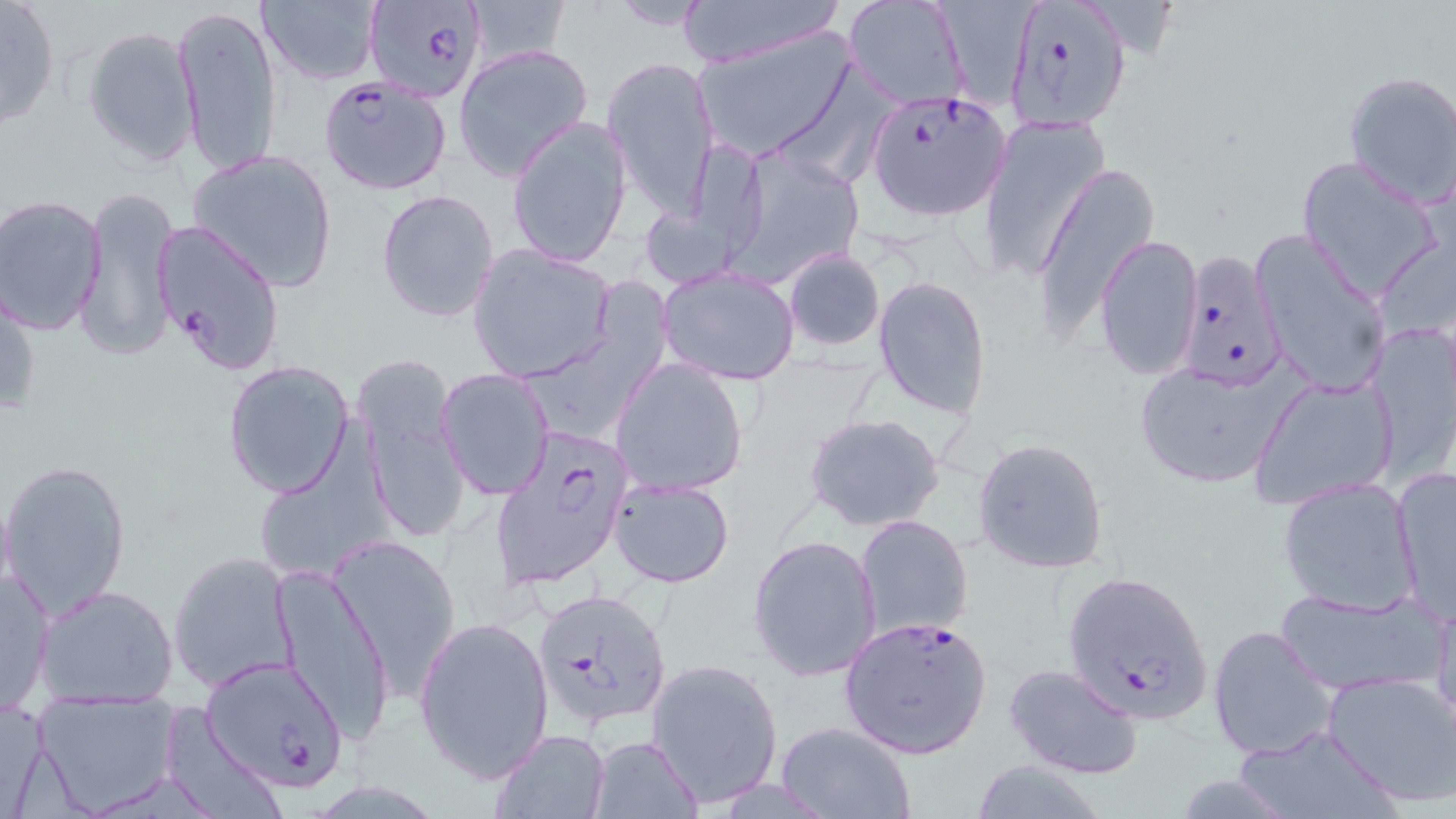

Summary:
  - Coordinate format: approximate bounding boxes as named x1/y1/x2/y2 corners in pixels
  - Uninfected red blood cell locations: (x1=0, y1=0, x2=62, y2=131), (x1=464, y1=0, x2=575, y2=66), (x1=606, y1=0, x2=715, y2=31), (x1=672, y1=0, x2=846, y2=68), (x1=842, y1=0, x2=972, y2=111), (x1=256, y1=1, x2=383, y2=86), (x1=930, y1=2, x2=1055, y2=113), (x1=172, y1=3, x2=282, y2=181), (x1=81, y1=25, x2=203, y2=168), (x1=694, y1=28, x2=857, y2=161), (x1=453, y1=45, x2=594, y2=180), (x1=603, y1=55, x2=720, y2=217), (x1=1342, y1=69, x2=1456, y2=206), (x1=978, y1=114, x2=1110, y2=286), (x1=506, y1=115, x2=633, y2=269), (x1=725, y1=147, x2=867, y2=286), (x1=186, y1=148, x2=339, y2=294), (x1=1297, y1=157, x2=1445, y2=298), (x1=1033, y1=161, x2=1159, y2=340), (x1=76, y1=185, x2=178, y2=359), (x1=376, y1=188, x2=501, y2=325), (x1=2, y1=195, x2=107, y2=334), (x1=1251, y1=231, x2=1388, y2=401), (x1=1096, y1=235, x2=1204, y2=381), (x1=468, y1=244, x2=617, y2=382), (x1=783, y1=249, x2=885, y2=351), (x1=658, y1=266, x2=800, y2=383), (x1=524, y1=273, x2=684, y2=454), (x1=873, y1=274, x2=991, y2=418), (x1=1, y1=279, x2=39, y2=418), (x1=1368, y1=322, x2=1456, y2=478), (x1=611, y1=358, x2=748, y2=497), (x1=223, y1=359, x2=355, y2=499), (x1=1131, y1=360, x2=1297, y2=490), (x1=437, y1=368, x2=557, y2=500), (x1=1248, y1=375, x2=1399, y2=509), (x1=360, y1=387, x2=468, y2=544), (x1=804, y1=412, x2=947, y2=534), (x1=972, y1=439, x2=1109, y2=574), (x1=2, y1=460, x2=132, y2=618), (x1=249, y1=460, x2=386, y2=584), (x1=1390, y1=466, x2=1455, y2=620), (x1=607, y1=476, x2=736, y2=588), (x1=1278, y1=476, x2=1422, y2=615), (x1=855, y1=514, x2=974, y2=639), (x1=748, y1=532, x2=882, y2=682), (x1=329, y1=533, x2=463, y2=696), (x1=169, y1=551, x2=300, y2=691), (x1=1, y1=565, x2=55, y2=716), (x1=272, y1=569, x2=393, y2=741), (x1=35, y1=585, x2=180, y2=708), (x1=1276, y1=586, x2=1442, y2=697), (x1=1430, y1=592, x2=1456, y2=734), (x1=413, y1=614, x2=554, y2=784), (x1=1207, y1=624, x2=1339, y2=762), (x1=645, y1=657, x2=784, y2=806), (x1=1005, y1=663, x2=1145, y2=780), (x1=1322, y1=670, x2=1456, y2=807), (x1=36, y1=693, x2=181, y2=811), (x1=1, y1=698, x2=52, y2=818), (x1=774, y1=720, x2=919, y2=818), (x1=1233, y1=725, x2=1398, y2=819), (x1=489, y1=729, x2=611, y2=818), (x1=588, y1=735, x2=702, y2=818), (x1=967, y1=758, x2=1111, y2=819)
  - Plasmodium falciparum-infected red blood cell locations: (x1=365, y1=0, x2=488, y2=102), (x1=1004, y1=0, x2=1130, y2=131), (x1=313, y1=80, x2=451, y2=196), (x1=868, y1=89, x2=1011, y2=217), (x1=151, y1=221, x2=285, y2=375), (x1=1175, y1=252, x2=1286, y2=390), (x1=488, y1=425, x2=638, y2=606), (x1=1059, y1=567, x2=1215, y2=727), (x1=533, y1=588, x2=671, y2=725), (x1=838, y1=615, x2=992, y2=758), (x1=203, y1=655, x2=349, y2=792)
  - Slide-level diagnosis: Plasmodium falciparum
  - Field of view: single
  - Magnification: 1000x
  - Preparation: thin blood film
  - Stain: May-Grünwald-Giemsa
  - Modality: optical microscopy
  - Image size: 1456×819 pixels